Assess for Plasmodium parasites.
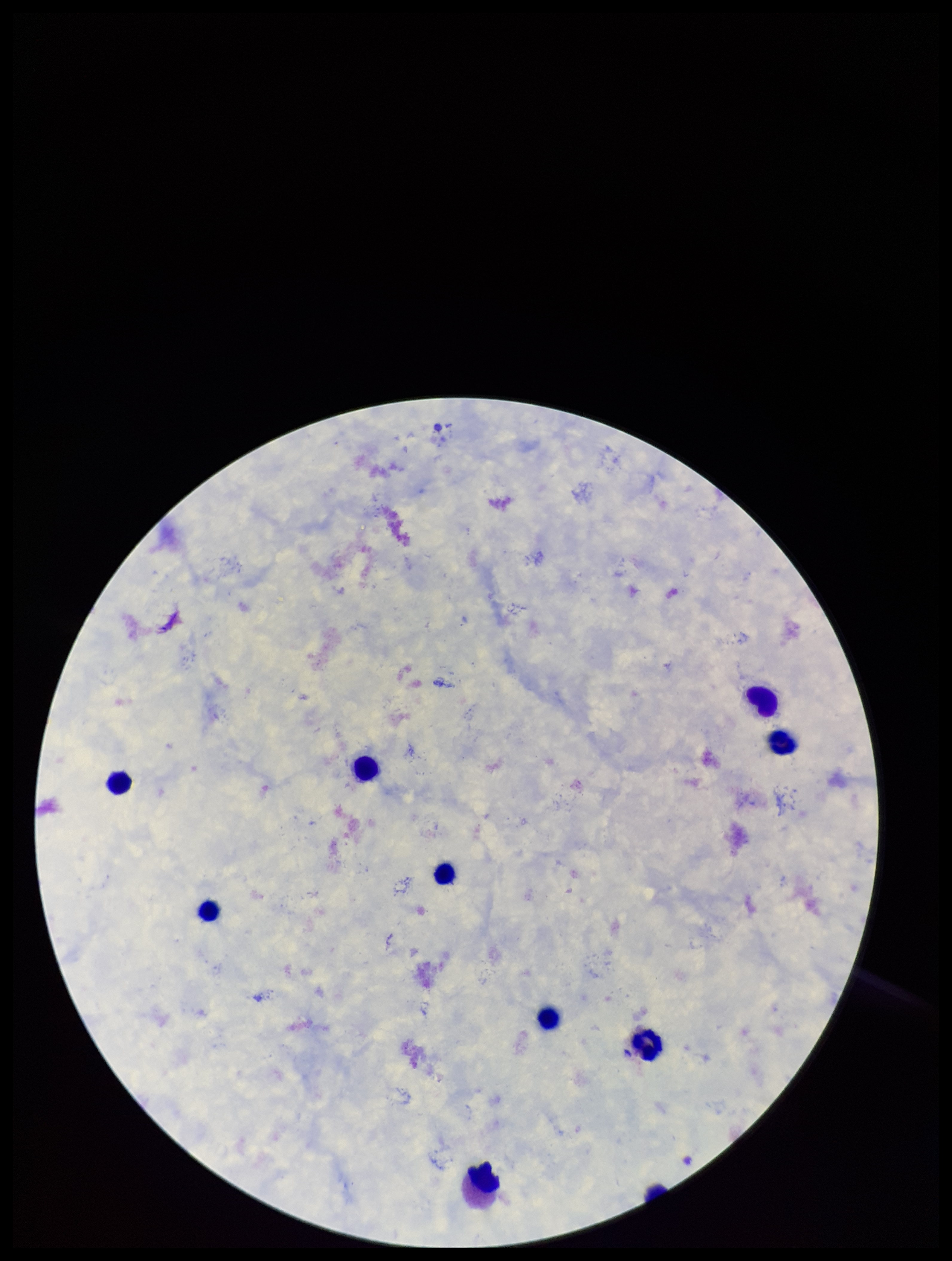

None detected.

Image is 952×1261 pixels. Photographed through the microscope eyepiece with a smartphone camera. Stained with Giemsa. Single field of view. Leukocyte count: 10. Patient malaria status: negative. Preparation: thick blood smear. Parasite count: 0.